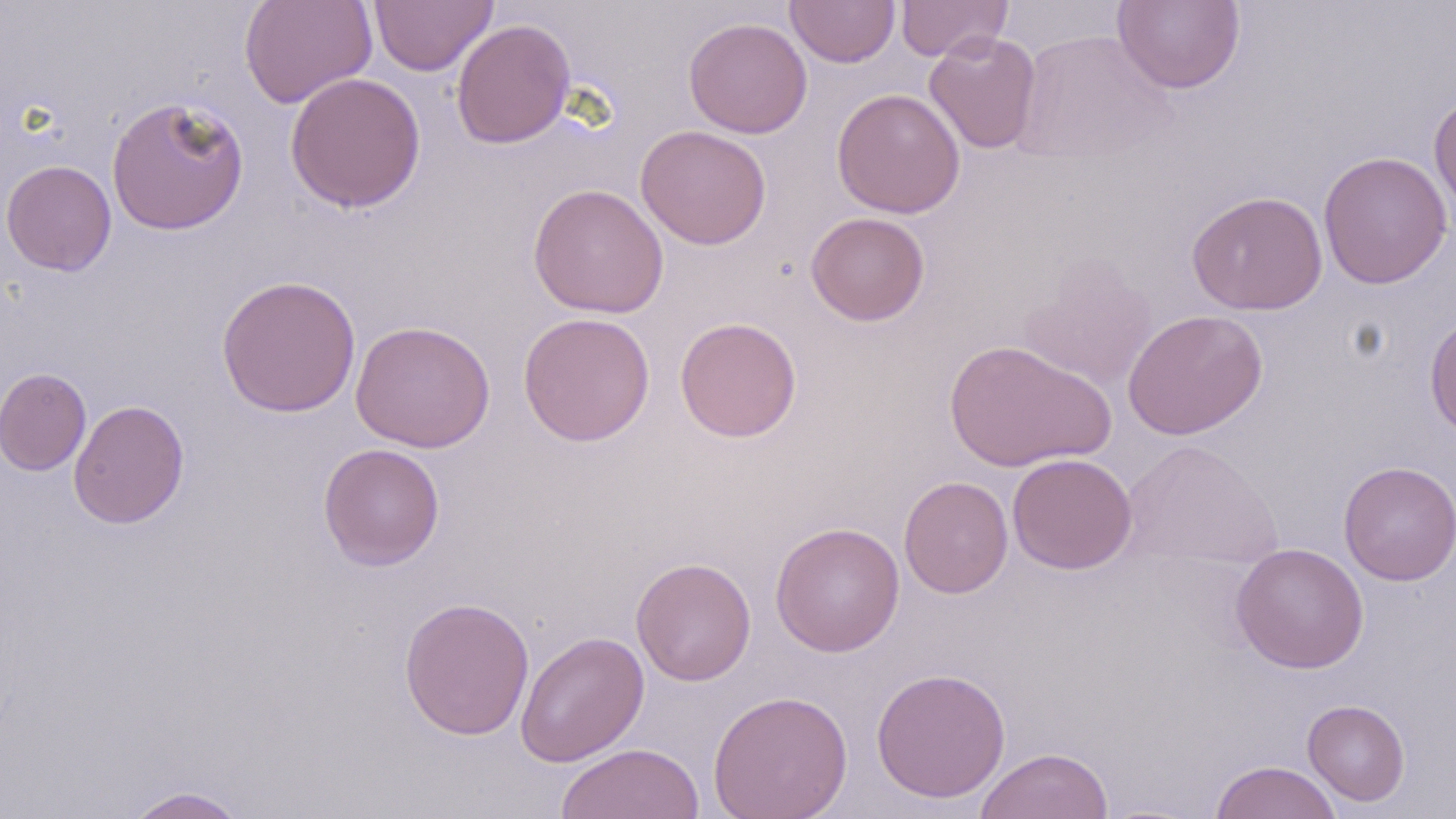

slide-level diagnosis = negative for blood parasites
magnification = 1000x
stain = May-Grünwald-Giemsa
uninfected red blood cell locations = approximate bounding boxes as [x1, y1, x2, y2] in pixels: [239, 0, 378, 109], [369, 0, 498, 76], [785, 0, 901, 67], [894, 0, 1012, 62], [1112, 1, 1246, 94], [683, 17, 812, 139], [451, 18, 576, 149], [1010, 29, 1176, 166], [923, 31, 1042, 154], [285, 71, 426, 213], [832, 88, 965, 218], [1429, 91, 1456, 220], [106, 95, 249, 236], [635, 124, 772, 250], [1317, 150, 1453, 290], [1, 159, 117, 276], [528, 183, 669, 318], [1187, 191, 1328, 315], [805, 212, 930, 326], [1018, 258, 1158, 392], [216, 275, 361, 418], [1123, 309, 1267, 440], [517, 311, 656, 447], [1424, 312, 1456, 440], [674, 317, 803, 442], [350, 320, 496, 453], [944, 339, 1115, 473], [0, 367, 91, 476], [68, 399, 189, 529], [1119, 438, 1283, 573], [318, 443, 445, 571], [1007, 452, 1137, 575], [1338, 460, 1456, 586], [898, 476, 1013, 599], [770, 521, 905, 657], [1231, 542, 1369, 673], [631, 556, 756, 686], [398, 596, 536, 740], [515, 630, 650, 767], [871, 667, 1011, 803], [707, 689, 853, 819], [1302, 699, 1410, 807], [556, 742, 705, 819], [975, 746, 1114, 819], [1209, 760, 1343, 819], [122, 785, 250, 818]
modality = optical microscopy
image size = 1456×819 pixels
preparation = thin blood film
field of view = single